Name the parasite shown.
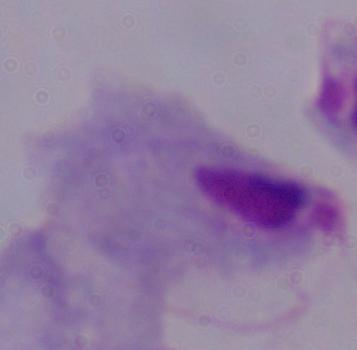
This is a trichomonad.

1000x magnification. Micrograph.